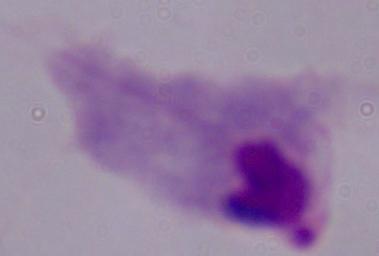
Photomicrograph. A trichomonad is seen. Captured at 1000x magnification.